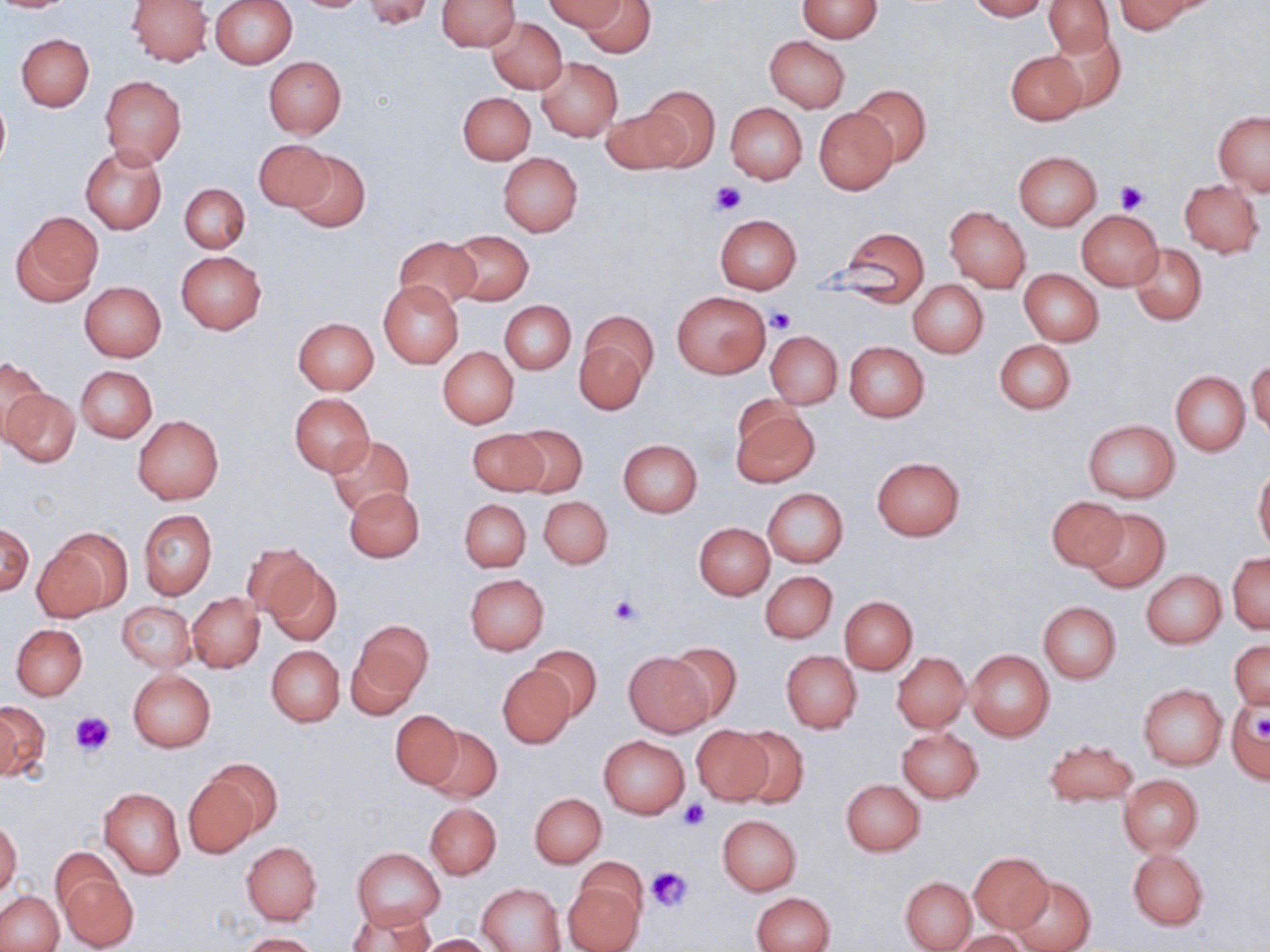 Approximate bounding boxes as (x1,y1)-(x2,y2) corner pairs in pixels. Uninfected red blood cell locations: (0,0)-(74,13), (128,0)-(212,66), (437,0)-(519,50), (545,0)-(624,32), (578,0)-(654,58), (798,0)-(882,42), (965,0)-(1049,21), (1115,0)-(1203,35), (211,1)-(297,69), (362,1)-(436,28), (1044,2)-(1113,56), (486,18)-(566,93), (1044,28)-(1125,112), (16,33)-(95,112), (765,37)-(850,112), (1005,50)-(1087,126), (263,56)-(346,137), (536,57)-(622,142), (100,75)-(187,169), (641,85)-(720,169), (852,85)-(931,166), (458,91)-(535,164), (0,92)-(9,174), (726,103)-(807,185), (603,106)-(687,177), (814,108)-(897,195), (1213,111)-(1270,196), (254,138)-(335,213), (81,146)-(168,234), (287,149)-(371,232), (1013,151)-(1101,229), (498,152)-(583,237), (1179,179)-(1264,256), (179,182)-(250,253), (945,207)-(1030,292), (1076,209)-(1163,290), (12,212)-(104,304), (714,214)-(802,293), (830,227)-(931,303), (450,229)-(534,305), (393,236)-(480,309), (1129,243)-(1208,326), (175,250)-(266,334), (1019,269)-(1103,346), (378,279)-(464,369), (908,281)-(988,358), (80,282)-(166,361), (672,291)-(771,378), (500,302)-(575,374), (580,310)-(661,385), (293,317)-(379,393), (575,331)-(651,414), (766,331)-(842,408), (994,340)-(1076,414), (844,341)-(929,422), (438,346)-(519,429), (0,356)-(49,445), (1248,358)-(1270,436), (75,365)-(157,443), (1170,371)-(1251,454), (1,388)-(80,467), (289,393)-(375,476), (730,403)-(819,487), (133,415)-(223,504), (1083,421)-(1179,503), (512,424)-(587,498), (469,430)-(547,496), (326,436)-(414,518), (618,439)-(703,517), (871,457)-(964,540), (1254,468)-(1270,553), (344,487)-(423,563), (763,488)-(848,567), (539,496)-(612,568), (1046,496)-(1126,573), (460,499)-(531,572), (1082,506)-(1171,593), (139,510)-(217,600), (0,523)-(34,596), (694,523)-(773,599), (39,531)-(127,620), (240,543)-(323,622), (1228,553)-(1269,634), (262,556)-(342,645), (1141,569)-(1226,648), (760,570)-(836,644), (465,574)-(549,655), (188,593)-(264,672), (840,596)-(917,673), (1037,601)-(1121,684), (118,602)-(195,671), (350,620)-(432,711), (12,624)-(88,700), (1229,639)-(1270,710), (665,641)-(743,724), (266,646)-(344,727), (529,646)-(603,722), (965,649)-(1055,742), (781,650)-(861,733), (626,652)-(714,736), (893,652)-(970,732), (498,667)-(574,748), (128,670)-(216,752), (1138,685)-(1226,769), (0,700)-(49,781), (1226,700)-(1270,785), (391,710)-(463,789), (692,724)-(773,805), (424,725)-(501,801), (732,725)-(810,807), (897,728)-(983,802), (598,735)-(689,818), (1044,739)-(1138,807), (204,758)-(281,842), (1118,774)-(1203,855), (183,775)-(262,857), (841,779)-(926,856), (99,787)-(186,879), (529,793)-(606,868), (425,802)-(501,879), (717,814)-(801,895), (0,821)-(21,895), (241,841)-(322,924), (1128,847)-(1209,930), (353,848)-(444,927), (969,852)-(1053,933), (575,858)-(649,923), (57,868)-(138,951), (901,876)-(977,951), (1010,876)-(1094,952), (563,878)-(645,952), (478,883)-(565,952), (0,891)-(63,952), (752,892)-(834,952), (349,907)-(434,952), (953,930)-(1031,952), (240,933)-(320,952), (413,933)-(495,952). Platelet locations: (709,181)-(747,215), (1115,181)-(1149,214), (766,306)-(796,334), (610,596)-(641,625), (70,710)-(117,755), (1252,714)-(1270,744), (680,799)-(710,830), (645,865)-(693,912). Slide-level diagnosis: negative for blood parasites. Optical microscopy. May-Grünwald-Giemsa stain. Image is 1270×952 pixels. Thin blood smear. One field of a larger specimen. 1000x magnification.